Describe the morphology of the erythrocytes.
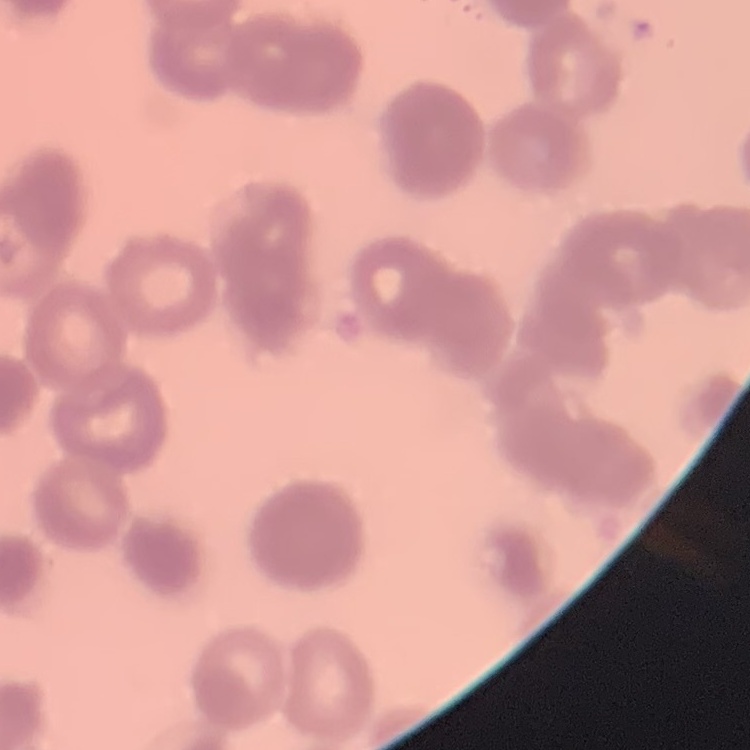

They show rouleaux formation.

Summary:
  - Stain: Field's or Giemsa
  - Image type: square crop of a larger photomicrograph
  - Preparation: thin blood film